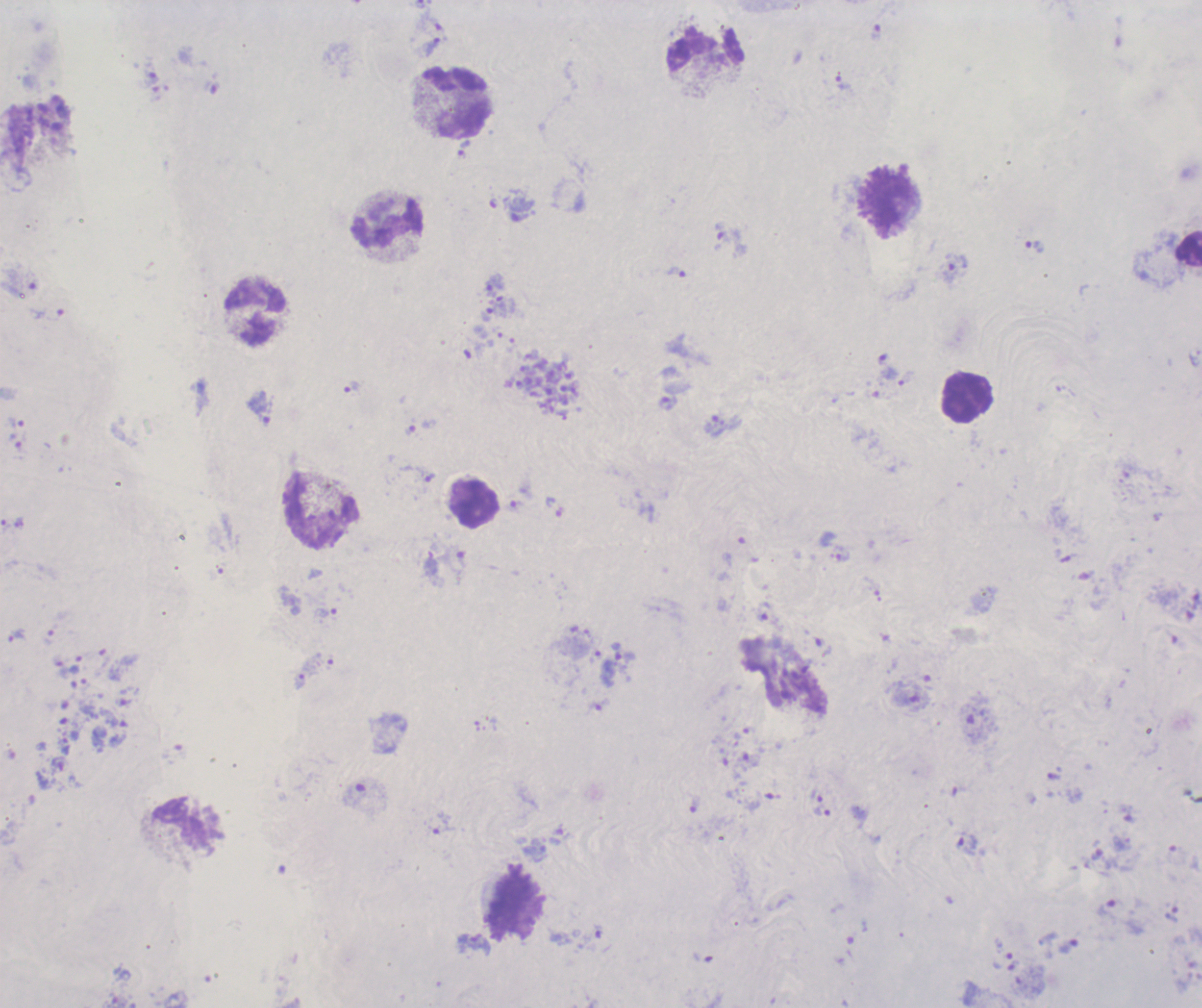

coordinate format = approximate centers as [x, y] in pixels
schizont locations = [547, 387]
leukocyte locations = [705, 49], [457, 103], [889, 202], [388, 225], [1189, 248], [254, 313], [968, 397], [474, 504], [321, 513], [188, 825], [515, 906]
trophozoite locations = [433, 47], [151, 79], [842, 83], [464, 148], [1035, 246], [676, 272], [495, 285], [487, 314], [887, 367], [351, 387], [668, 404], [260, 407], [16, 423], [715, 425], [840, 554], [763, 611], [326, 612], [17, 636], [623, 653], [823, 811], [966, 845], [472, 943], [1069, 946]
life-cycle stages observed = trophozoite, schizont
magnification = 100x
preparation = thick blood smear
image size = 1202×1008 pixels
field of view = one from this slide
background quality = poor
context = previously used in a real diagnosis
stain = Romanowsky
result = Plasmodium parasites detected